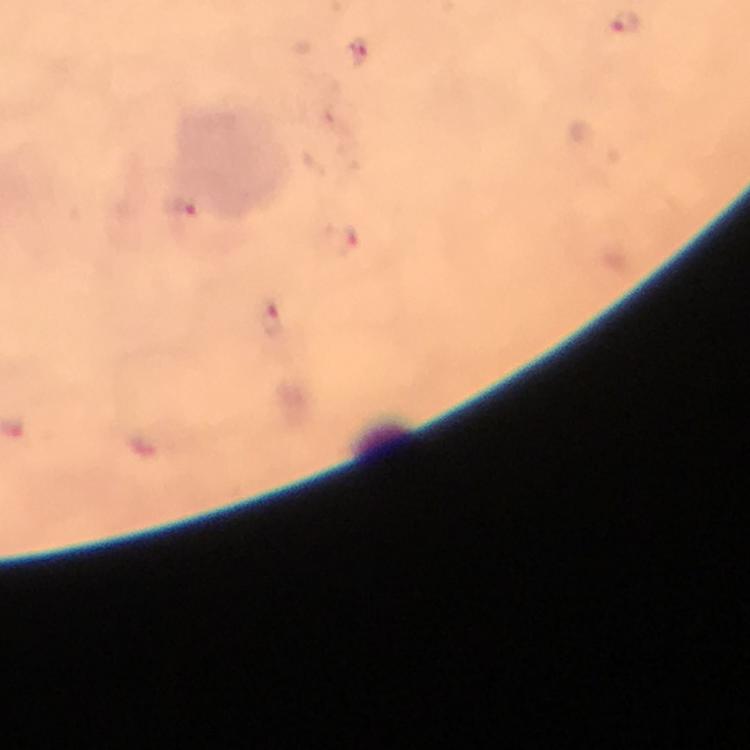
Approximate object centers, in pixels from the top-left corner. Malaria parasite locations: (x=626, y=21), (x=359, y=51), (x=181, y=208), (x=346, y=241), (x=271, y=319). 100x magnification. Image is 750×750 pixels. A crop from one field of view. Immersion oil applied. Thick blood smear. From a malaria diagnostic workup. Smartphone photograph taken through a microscope. Giemsa-stained preparation.